Point out each malaria parasite.
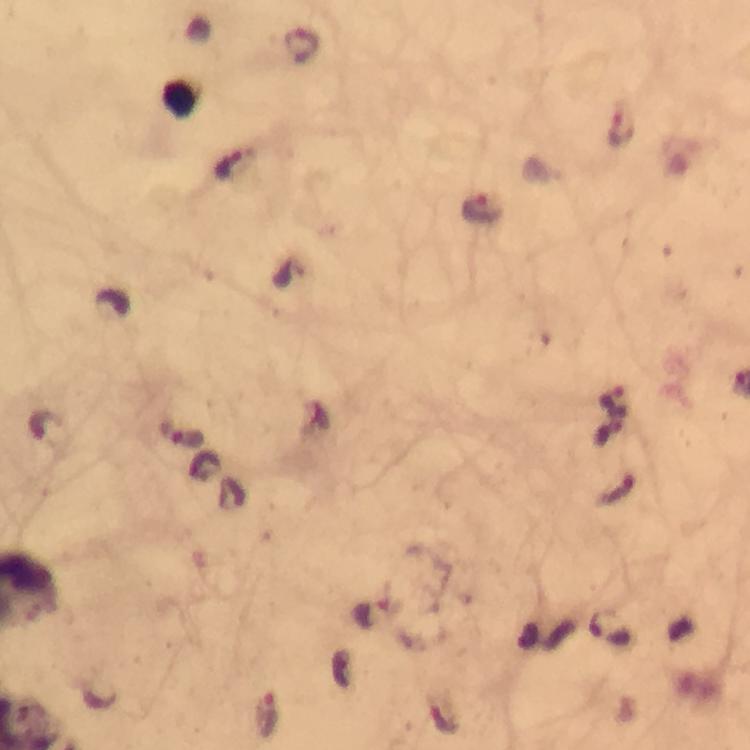

Approximate object centers, in pixels from the top-left corner.
Malaria parasites: (x=621, y=126), (x=233, y=163), (x=482, y=208), (x=615, y=402), (x=608, y=431), (x=372, y=613), (x=610, y=631), (x=266, y=717), (x=443, y=718).

Summary:
  - Stain: Giemsa
  - Immersion oil: applied
  - Capture: smartphone camera through the microscope
  - Magnification: 100x
  - Cropped from: one field of view
  - Image size: 750×750 pixels
  - Context: from a diagnostic examination for malaria
  - Preparation: thick smear